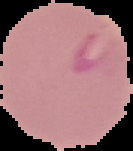
Summary:
  - Preparation: thin blood film
  - Image type: segmented cell region with the area outside set to black
  - Result: Plasmodium parasites identified
  - Image size: 133×151 pixels